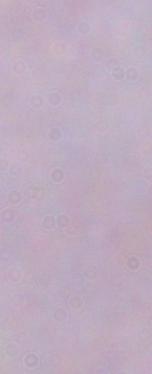
modality = photomicrograph
identification = trypanosome
magnification = 1000x